Locate every blood parasite and identify its species.
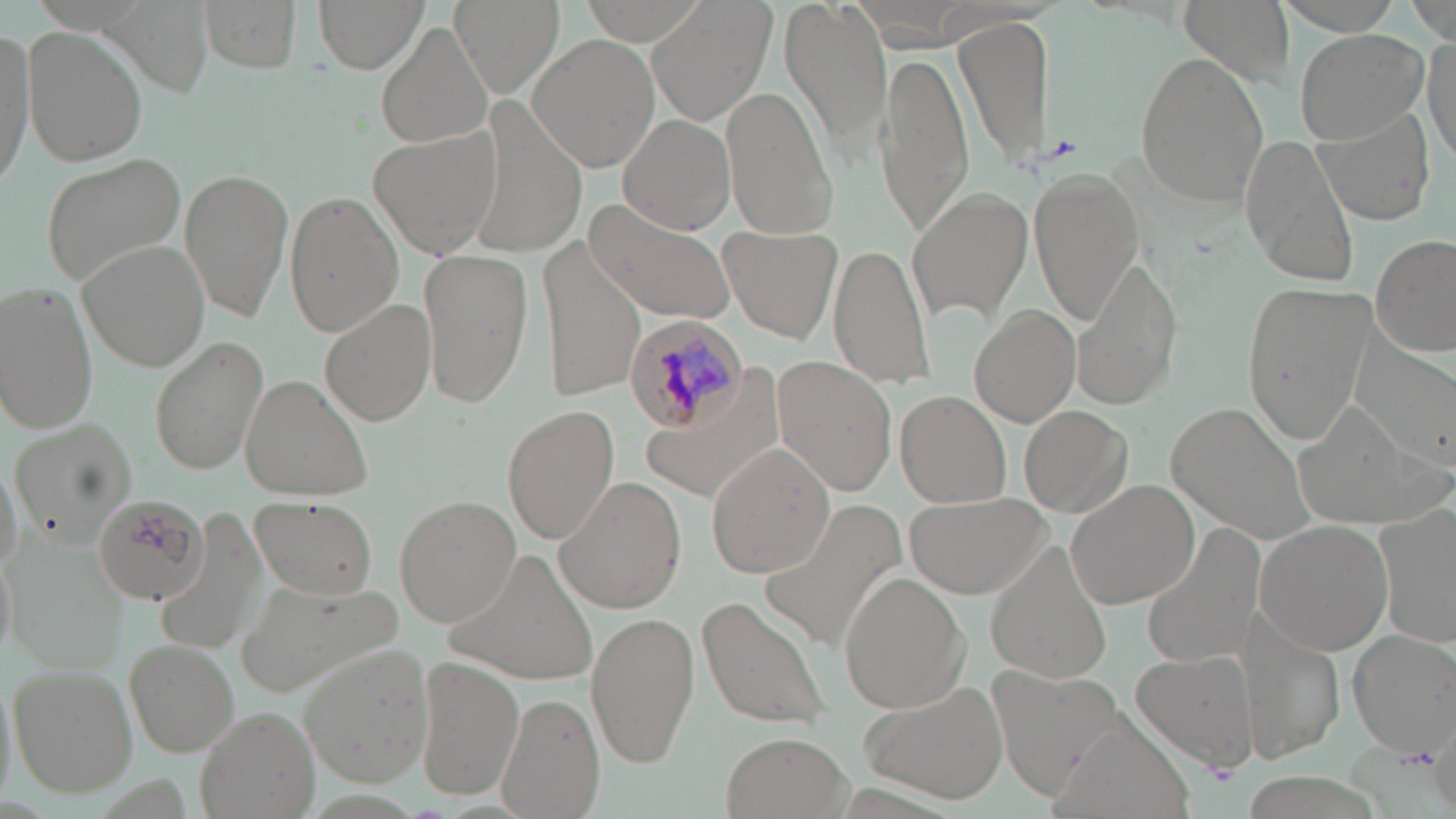
Approximate bounding boxes as named x1/y1/x2/y2 corners in pixels.
Plasmodium malariae-infected red blood cells: (x1=622, y1=314, x2=748, y2=434).
No Plasmodium falciparum, Plasmodium ovale, Plasmodium vivax, Babesia divergens, or Trypanosoma brucei observed.

{
  "slide_level_diagnosis": "Plasmodium malariae",
  "stain": "May-Grünwald-Giemsa",
  "uninfected_red_blood_cell_locations": "approximate bounding boxes as named x1/y1/x2/y2 corners in pixels: (x1=104, y1=0, x2=214, y2=99), (x1=199, y1=0, x2=305, y2=74), (x1=313, y1=0, x2=430, y2=74), (x1=451, y1=0, x2=564, y2=99), (x1=580, y1=0, x2=708, y2=45), (x1=780, y1=0, x2=892, y2=149), (x1=1179, y1=0, x2=1296, y2=86), (x1=1274, y1=0, x2=1410, y2=34), (x1=650, y1=2, x2=774, y2=125), (x1=1410, y1=2, x2=1456, y2=42), (x1=956, y1=13, x2=1054, y2=170), (x1=375, y1=21, x2=493, y2=149), (x1=0, y1=24, x2=36, y2=192), (x1=21, y1=25, x2=150, y2=166), (x1=1293, y1=28, x2=1430, y2=144), (x1=529, y1=34, x2=661, y2=173), (x1=1424, y1=35, x2=1455, y2=166), (x1=1134, y1=50, x2=1270, y2=209), (x1=875, y1=51, x2=975, y2=232), (x1=720, y1=88, x2=839, y2=240), (x1=1313, y1=107, x2=1436, y2=226), (x1=617, y1=113, x2=737, y2=235), (x1=367, y1=127, x2=501, y2=262), (x1=1244, y1=134, x2=1363, y2=287), (x1=43, y1=152, x2=190, y2=284), (x1=1029, y1=166, x2=1140, y2=327), (x1=180, y1=167, x2=294, y2=323), (x1=908, y1=188, x2=1033, y2=324), (x1=285, y1=190, x2=403, y2=336), (x1=587, y1=199, x2=742, y2=326), (x1=718, y1=226, x2=842, y2=343), (x1=1371, y1=235, x2=1456, y2=357), (x1=78, y1=240, x2=210, y2=372), (x1=541, y1=240, x2=644, y2=399), (x1=826, y1=241, x2=937, y2=390), (x1=417, y1=248, x2=536, y2=410), (x1=1068, y1=257, x2=1183, y2=410), (x1=1, y1=280, x2=100, y2=432), (x1=1239, y1=280, x2=1377, y2=446), (x1=318, y1=298, x2=436, y2=427), (x1=970, y1=306, x2=1082, y2=427), (x1=1349, y1=330, x2=1456, y2=468), (x1=152, y1=336, x2=269, y2=474), (x1=772, y1=357, x2=898, y2=496), (x1=239, y1=372, x2=373, y2=500), (x1=894, y1=389, x2=1014, y2=508), (x1=1173, y1=401, x2=1319, y2=543), (x1=1288, y1=401, x2=1448, y2=536), (x1=1022, y1=402, x2=1136, y2=517), (x1=503, y1=405, x2=619, y2=546), (x1=11, y1=416, x2=140, y2=546), (x1=706, y1=445, x2=836, y2=577), (x1=555, y1=477, x2=687, y2=615), (x1=1065, y1=480, x2=1200, y2=610), (x1=902, y1=490, x2=1052, y2=599), (x1=249, y1=495, x2=379, y2=600), (x1=394, y1=495, x2=521, y2=626), (x1=759, y1=497, x2=907, y2=652), (x1=157, y1=508, x2=270, y2=658), (x1=1375, y1=510, x2=1456, y2=647), (x1=1255, y1=521, x2=1394, y2=656), (x1=1140, y1=530, x2=1264, y2=668), (x1=985, y1=540, x2=1114, y2=685), (x1=0, y1=545, x2=16, y2=661), (x1=446, y1=545, x2=602, y2=683), (x1=837, y1=572, x2=970, y2=712), (x1=237, y1=577, x2=407, y2=698), (x1=695, y1=594, x2=831, y2=735), (x1=586, y1=610, x2=699, y2=768), (x1=1346, y1=629, x2=1455, y2=758), (x1=125, y1=639, x2=239, y2=757), (x1=299, y1=644, x2=437, y2=786), (x1=1129, y1=651, x2=1259, y2=773), (x1=413, y1=655, x2=524, y2=803), (x1=8, y1=663, x2=139, y2=797), (x1=989, y1=667, x2=1125, y2=793), (x1=863, y1=680, x2=1009, y2=804), (x1=498, y1=690, x2=603, y2=819), (x1=193, y1=706, x2=321, y2=819), (x1=1049, y1=718, x2=1194, y2=819), (x1=720, y1=730, x2=849, y2=819)",
  "modality": "optical microscopy",
  "field_of_view": "single",
  "magnification": "1000x",
  "image_size": "1456×819 pixels",
  "platelet_locations": "approximate bounding boxes as named x1/y1/x2/y2 corners in pixels: (x1=1039, y1=133, x2=1084, y2=166), (x1=1398, y1=745, x2=1439, y2=773)",
  "preparation": "thin blood film"
}